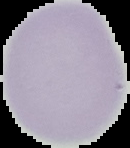
Summary:
  - Malaria status: uninfected
  - Image type: cell region segmented out of the field of view; surrounding area masked to black
  - Image size: 130×148 pixels
  - Preparation: thin blood smear